Name the cell type shown.
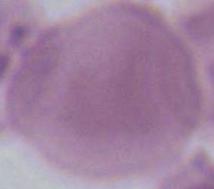
This is an erythrocyte.

Photomicrograph. 1000x magnification.